State which cell type is depicted.
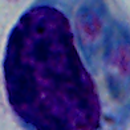

A leukocyte.

modality = micrograph
magnification = 1000x